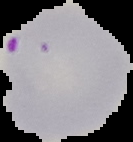

Summary:
  - Result: Plasmodium parasites identified
  - Image size: 133×142 pixels
  - Image type: cell region segmented out of the field of view; surrounding area masked to black
  - Preparation: thin blood smear